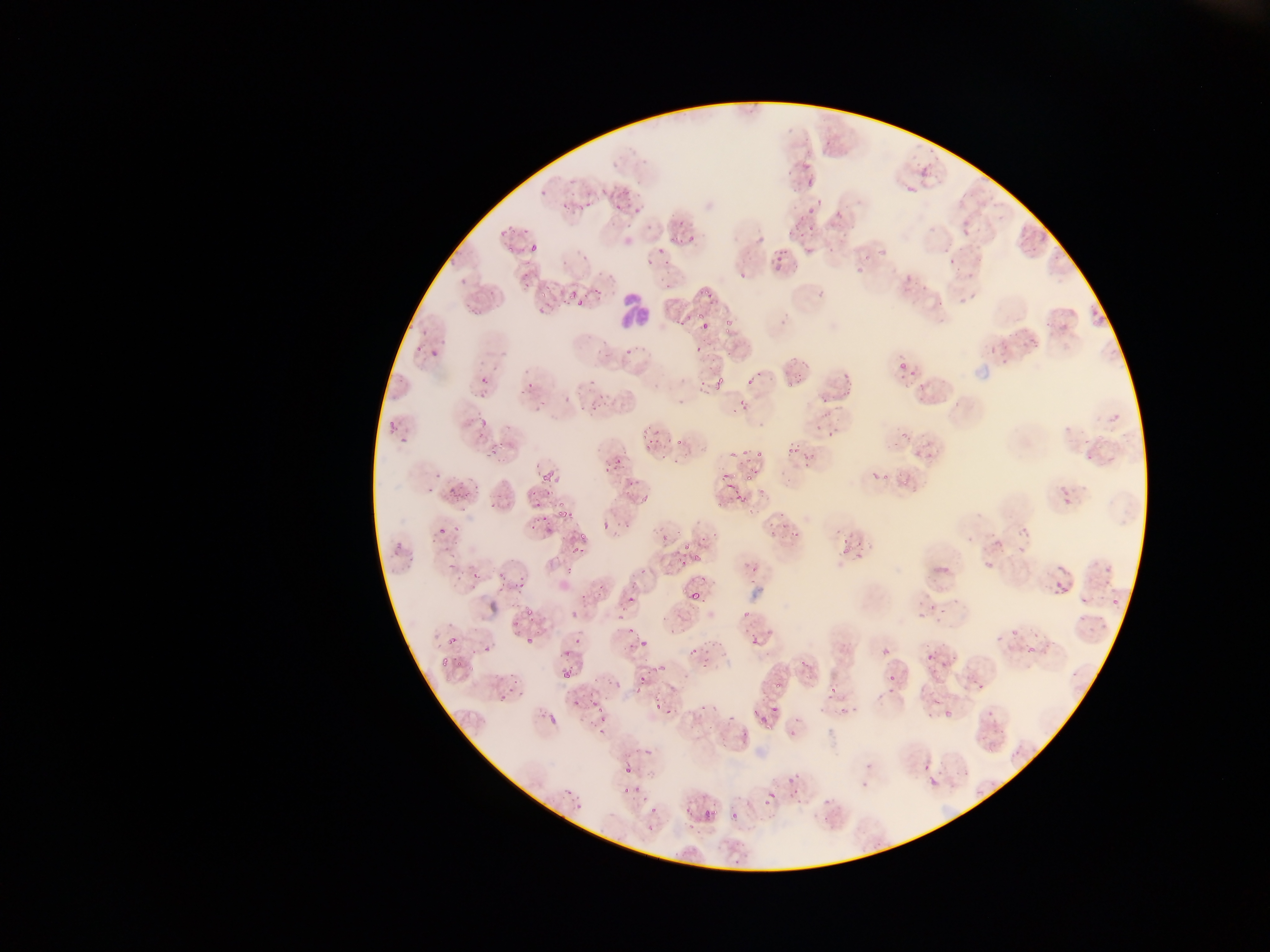

image size = 1270×952 pixels
preparation = thin blood smear
capture = mobile-phone photograph through a microscope
country = Ghana
leukocyte locations = approximate bounding boxes as [left, top, right, bottom] in pixels: [610, 290, 660, 337]
field of view = single
malaria parasite locations = approximate bounding boxes as [left, top, right, bottom] in pixels: [793, 158, 828, 184], [900, 169, 933, 199], [628, 183, 652, 220], [600, 188, 611, 196], [803, 199, 828, 217], [834, 199, 853, 221], [669, 211, 696, 241], [799, 211, 814, 238], [956, 222, 967, 239], [518, 227, 541, 262], [848, 242, 885, 279], [640, 244, 672, 267], [942, 244, 966, 267], [874, 246, 890, 265], [769, 247, 791, 275], [736, 255, 766, 280], [511, 264, 539, 286], [899, 272, 915, 289], [562, 274, 593, 310], [920, 277, 933, 288], [695, 284, 723, 307], [954, 285, 986, 312], [1087, 302, 1111, 322], [1049, 306, 1080, 340], [700, 321, 710, 332], [1017, 327, 1039, 350], [417, 329, 439, 363], [598, 340, 618, 355], [895, 346, 920, 372], [995, 350, 1005, 363], [793, 360, 810, 379], [704, 365, 730, 390], [742, 365, 760, 382], [452, 369, 482, 406], [836, 370, 859, 392], [822, 382, 830, 395], [548, 386, 576, 406], [591, 386, 620, 411], [730, 399, 738, 407], [385, 408, 402, 440], [487, 428, 520, 452], [736, 428, 765, 460], [899, 429, 910, 447], [783, 436, 800, 455], [674, 437, 683, 445], [910, 439, 927, 455], [1076, 452, 1096, 470], [802, 453, 812, 463], [450, 460, 475, 488], [537, 464, 555, 487], [868, 464, 887, 483], [630, 476, 666, 506], [728, 477, 758, 500], [523, 484, 542, 507], [1058, 486, 1080, 510], [441, 487, 463, 500], [478, 490, 501, 510], [548, 500, 578, 525], [425, 511, 453, 531], [533, 515, 544, 532], [1014, 515, 1036, 547], [694, 516, 728, 550], [444, 520, 461, 550], [389, 522, 412, 555], [838, 526, 863, 553], [785, 528, 802, 541], [570, 530, 588, 554], [546, 531, 577, 560], [675, 538, 697, 568], [980, 548, 997, 568], [462, 553, 497, 580], [1102, 562, 1113, 576], [503, 563, 532, 600], [1053, 577, 1065, 593], [617, 581, 648, 608], [571, 587, 597, 623], [690, 592, 699, 601], [935, 592, 955, 618], [1111, 597, 1119, 604], [915, 600, 930, 615], [741, 601, 758, 617], [616, 607, 635, 637], [670, 614, 689, 632], [515, 618, 544, 652], [996, 625, 1011, 644], [749, 631, 766, 648], [427, 634, 465, 667], [688, 634, 715, 660], [630, 638, 646, 650], [1022, 639, 1039, 659], [882, 649, 890, 657], [936, 649, 955, 672], [634, 656, 656, 682], [562, 669, 571, 678], [497, 674, 532, 701], [888, 674, 897, 682], [822, 677, 840, 699], [975, 679, 986, 688], [652, 681, 679, 713], [771, 681, 780, 694], [838, 697, 858, 724], [695, 698, 723, 719], [588, 700, 608, 737], [769, 706, 781, 718], [986, 706, 995, 715], [754, 707, 768, 724], [549, 714, 557, 725], [941, 715, 951, 721], [738, 727, 753, 738], [788, 729, 798, 737], [972, 730, 995, 765], [919, 749, 940, 771], [620, 752, 647, 777], [854, 773, 875, 795], [923, 773, 940, 794], [625, 780, 644, 797], [791, 781, 804, 798], [763, 787, 780, 809], [563, 788, 571, 796], [641, 796, 670, 818], [811, 806, 825, 826], [703, 809, 716, 821], [730, 811, 738, 820], [684, 841, 707, 864] | approximate [x, y] pixel centers of objects too small to bound: [765, 528], [745, 570], [928, 656]